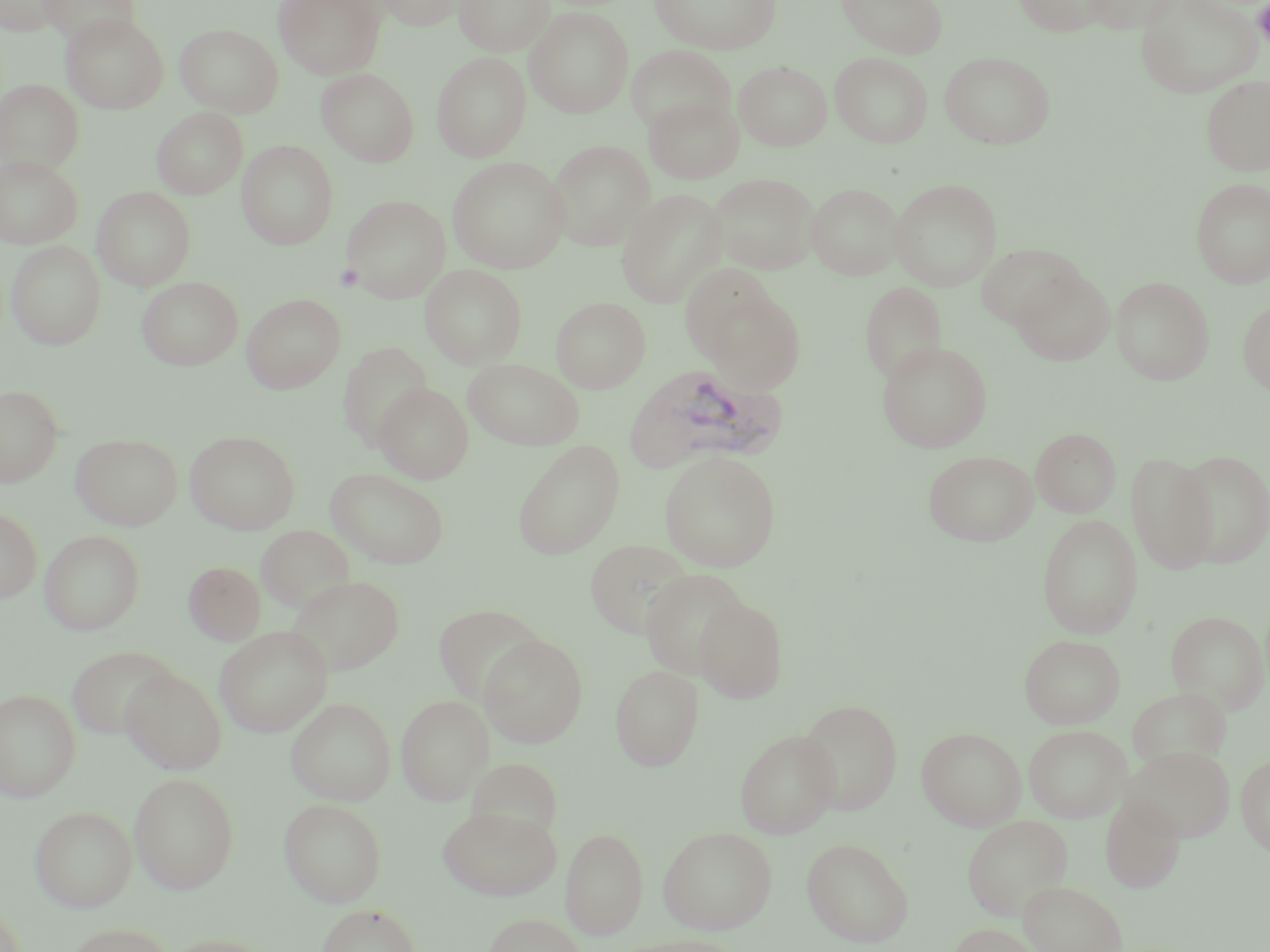 Approximate bounding boxes as [x1, y1, x2, y2] in pixels. Uninfected red blood cell locations: [0, 0, 65, 35], [39, 0, 140, 47], [273, 0, 386, 79], [371, 0, 470, 30], [455, 0, 554, 55], [650, 0, 781, 54], [836, 0, 947, 58], [1012, 0, 1112, 35], [1081, 0, 1181, 31], [1135, 0, 1263, 97], [526, 7, 633, 118], [62, 13, 169, 113], [175, 24, 283, 116], [625, 45, 734, 134], [939, 51, 1056, 148], [432, 52, 531, 162], [830, 53, 933, 148], [734, 61, 832, 150], [317, 69, 418, 166], [1201, 74, 1270, 177], [0, 79, 84, 175], [644, 94, 745, 184], [152, 107, 248, 199], [237, 140, 338, 249], [547, 140, 654, 250], [0, 155, 83, 248], [447, 157, 569, 273], [709, 173, 820, 275], [1191, 178, 1270, 287], [889, 179, 1003, 291], [806, 183, 904, 280], [92, 186, 196, 290], [616, 189, 728, 308], [342, 195, 451, 302], [6, 240, 106, 350], [975, 244, 1084, 330], [420, 264, 526, 368], [680, 264, 779, 362], [1010, 266, 1115, 366], [1111, 276, 1215, 385], [137, 277, 243, 370], [860, 281, 947, 385], [702, 287, 807, 394], [242, 293, 346, 393], [551, 296, 650, 393], [1238, 298, 1270, 398], [338, 341, 433, 449], [876, 341, 992, 452], [464, 359, 584, 450], [374, 383, 474, 483], [0, 384, 63, 486], [1031, 427, 1121, 518], [185, 430, 300, 534], [71, 433, 183, 530], [512, 440, 625, 559], [1175, 449, 1270, 567], [659, 450, 781, 571], [923, 450, 1038, 545], [1126, 451, 1218, 573], [326, 467, 451, 569], [0, 508, 42, 603], [1037, 514, 1142, 638], [256, 525, 354, 614], [40, 530, 145, 635], [586, 538, 694, 639], [183, 561, 266, 645], [640, 568, 751, 679], [286, 574, 404, 675], [694, 596, 788, 703], [432, 604, 548, 706], [1166, 611, 1269, 714], [215, 626, 332, 737], [478, 634, 588, 747], [1020, 634, 1125, 728], [65, 645, 181, 739], [610, 665, 703, 770], [122, 668, 226, 775], [1127, 687, 1231, 771], [0, 689, 81, 802], [397, 695, 493, 804], [286, 697, 396, 805], [797, 699, 903, 814], [1023, 724, 1131, 823], [917, 727, 1026, 831], [736, 729, 840, 838], [1122, 745, 1235, 841], [1236, 754, 1270, 856], [465, 756, 565, 844], [129, 772, 240, 894], [1100, 796, 1185, 894], [279, 798, 386, 906], [437, 804, 562, 900], [30, 805, 137, 912], [962, 815, 1074, 921], [658, 826, 778, 935], [561, 827, 648, 938], [801, 837, 914, 947], [1018, 880, 1128, 952], [316, 904, 423, 952], [481, 914, 588, 952], [63, 923, 177, 951], [946, 923, 1044, 952], [159, 934, 277, 952], [614, 935, 744, 952]. Platelet locations: [1254, 1, 1270, 48], [334, 263, 364, 292]. Plasmodium vivax-infected red blood cell locations: [628, 364, 789, 472]. Slide-level diagnosis: Plasmodium vivax. Thin blood smear. May-Grünwald-Giemsa stain. Single field of view. Light microscopy. Image is 1270×952 pixels. 1000x magnification.